Comment on the morphology of the red blood cells.
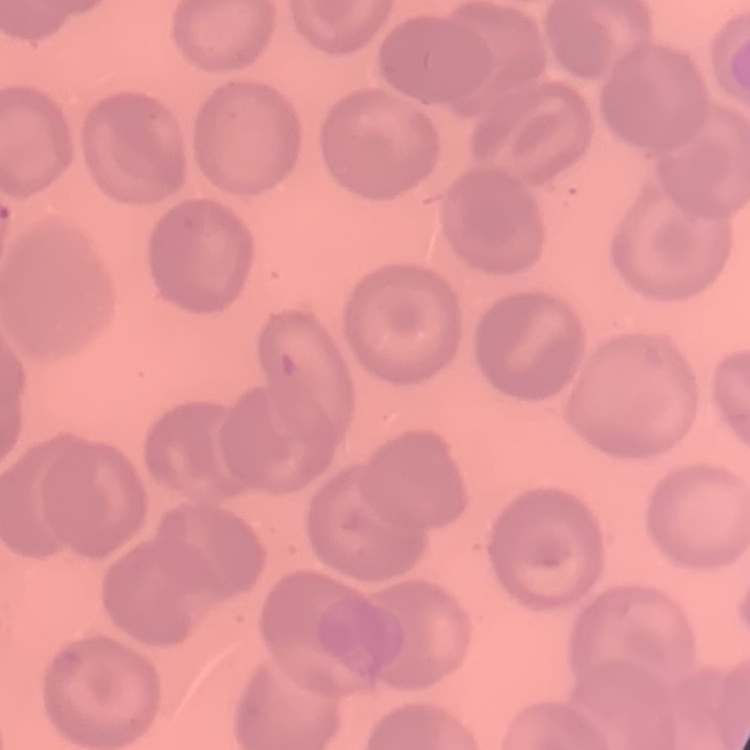
They show no rouleaux formation.

Thin peripheral smear. Field's or Giemsa stain. One tile cut from a larger photomicrograph.